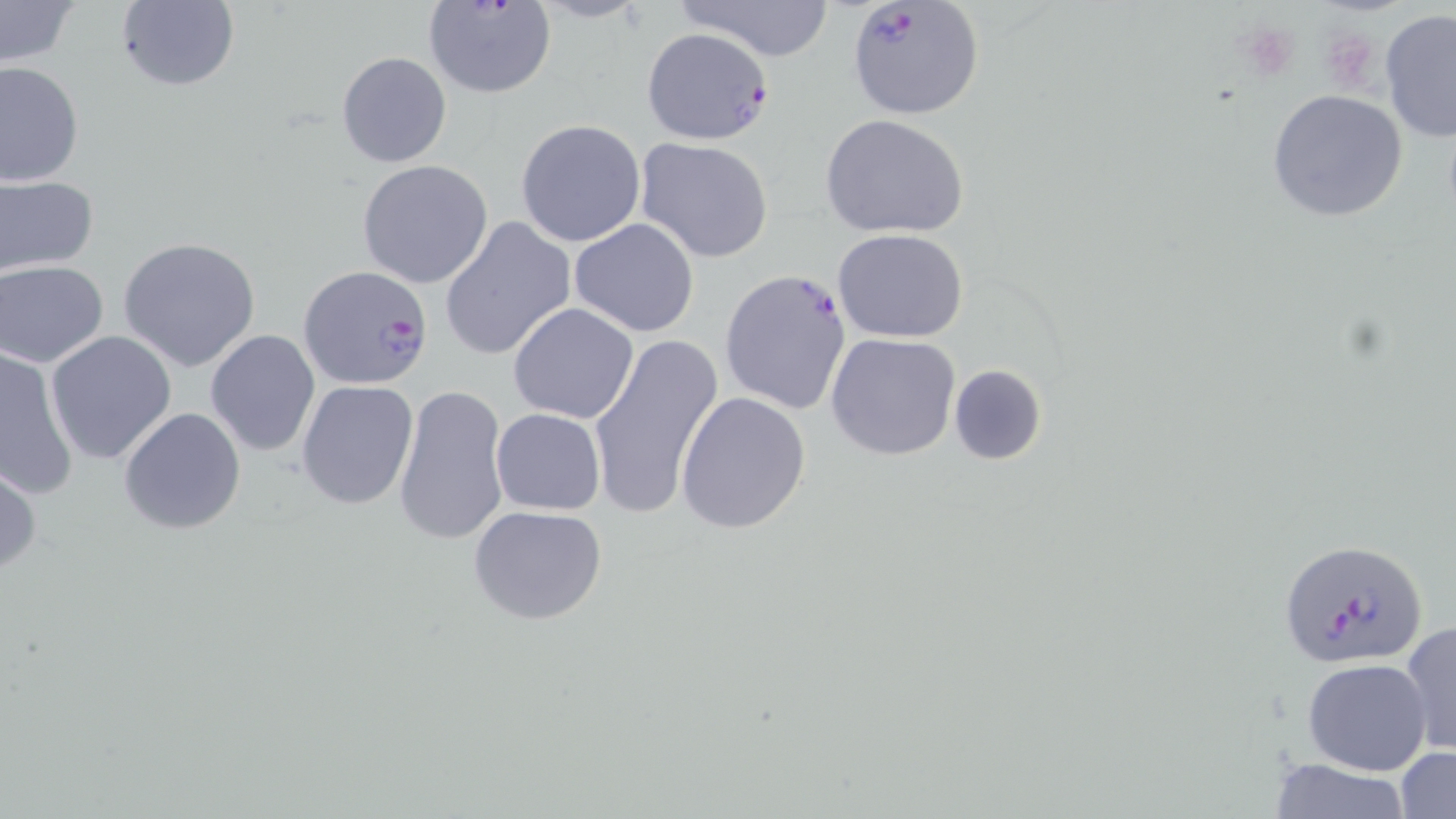

slide-level diagnosis = Plasmodium falciparum
magnification = 1000x
platelet locations = approximate bounding boxes as named x1/y1/x2/y2 corners in pixels: (x1=1239, y1=21, x2=1302, y2=82), (x1=1320, y1=27, x2=1379, y2=91)
image size = 1456×819 pixels
field of view = one of a larger specimen
stain = May-Grünwald-Giemsa
Plasmodium falciparum-infected red blood cell locations = approximate bounding boxes as named x1/y1/x2/y2 corners in pixels: (x1=423, y1=0, x2=555, y2=98), (x1=845, y1=0, x2=987, y2=119), (x1=641, y1=27, x2=773, y2=147), (x1=298, y1=264, x2=435, y2=391), (x1=720, y1=269, x2=853, y2=416), (x1=1278, y1=537, x2=1430, y2=668)
modality = optical microscopy
preparation = thin blood film
uninfected red blood cell locations = approximate bounding boxes as named x1/y1/x2/y2 corners in pixels: (x1=0, y1=0, x2=79, y2=70), (x1=113, y1=0, x2=240, y2=93), (x1=671, y1=0, x2=837, y2=62), (x1=1379, y1=11, x2=1456, y2=142), (x1=336, y1=50, x2=451, y2=168), (x1=0, y1=61, x2=83, y2=186), (x1=1265, y1=90, x2=1410, y2=224), (x1=821, y1=114, x2=970, y2=241), (x1=515, y1=118, x2=647, y2=249), (x1=635, y1=137, x2=773, y2=263), (x1=356, y1=159, x2=494, y2=288), (x1=0, y1=177, x2=98, y2=275), (x1=439, y1=215, x2=578, y2=361), (x1=569, y1=218, x2=699, y2=337), (x1=831, y1=228, x2=970, y2=344), (x1=117, y1=237, x2=263, y2=372), (x1=1, y1=260, x2=110, y2=366), (x1=508, y1=302, x2=640, y2=424), (x1=205, y1=330, x2=320, y2=458), (x1=46, y1=331, x2=178, y2=466), (x1=587, y1=331, x2=725, y2=519), (x1=826, y1=331, x2=962, y2=461), (x1=0, y1=346, x2=80, y2=498), (x1=948, y1=364, x2=1047, y2=466), (x1=296, y1=379, x2=419, y2=511), (x1=393, y1=383, x2=510, y2=546), (x1=675, y1=391, x2=811, y2=534), (x1=118, y1=406, x2=247, y2=537), (x1=490, y1=407, x2=605, y2=515), (x1=0, y1=459, x2=42, y2=581), (x1=468, y1=504, x2=607, y2=626), (x1=1400, y1=621, x2=1455, y2=757), (x1=1301, y1=658, x2=1431, y2=775), (x1=1395, y1=746, x2=1456, y2=819), (x1=1265, y1=758, x2=1413, y2=817)